Locate every P. falciparum parasite and give its life-cycle stage, and locate every leukocyte and any debris.
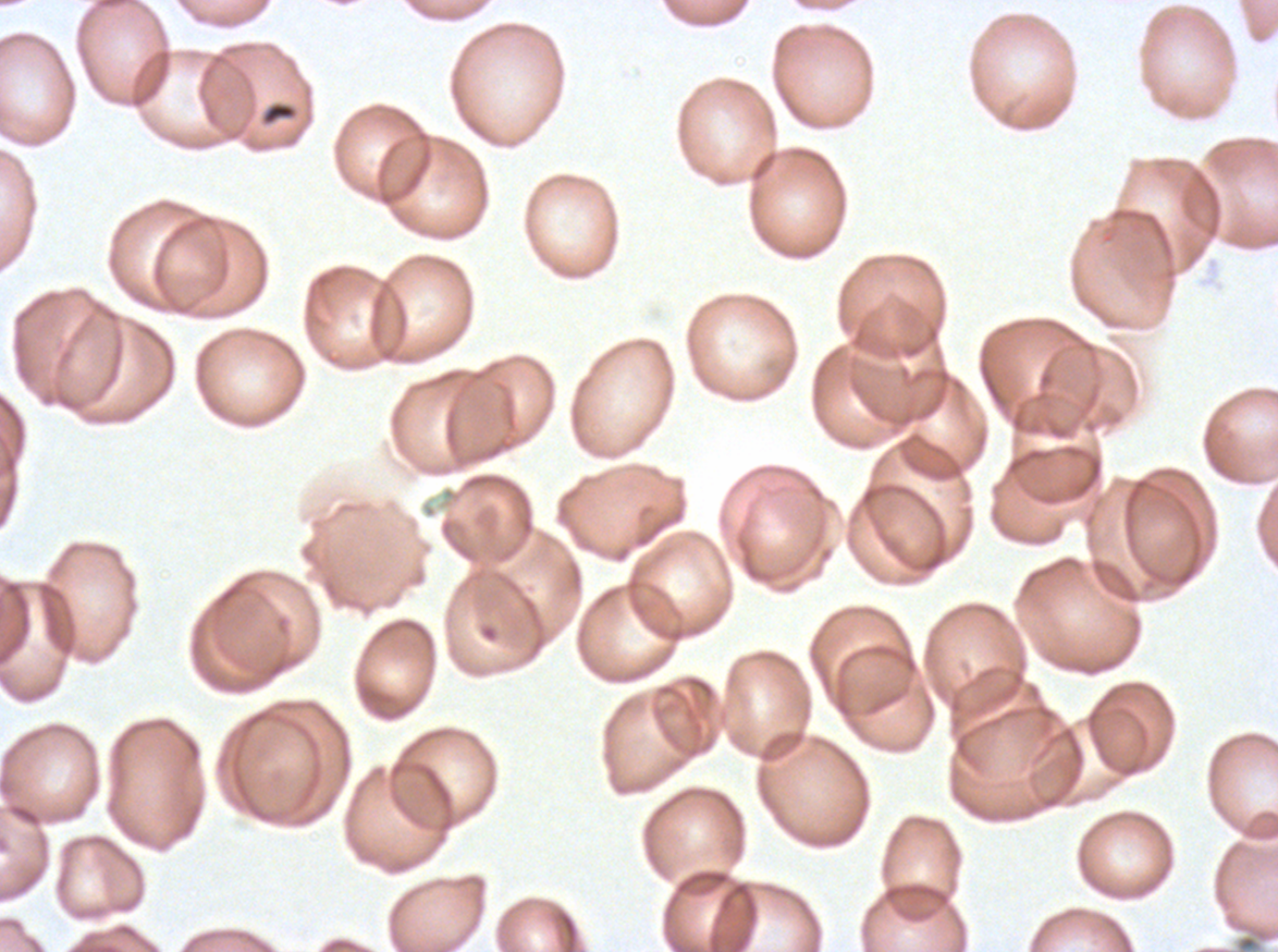
Approximate bounding boxes as {x1, y1, x2, y2} in pixels.
Debris: {259, 100, 300, 128}.
No rings, late-ring/early-trophozoite forms, mid trophozoites, late trophozoites, early schizonts, late schizonts, segmenters, gametocytes, or leukocytes observed.

Giemsa-stained preparation. Ex-vivo P. falciparum culture from a patient in The Gambia, grown for 24 to 48 hours. Image is 1278×952 pixels. Thin blood smear. A sub-image separated from a larger composite.